Report the malaria status.
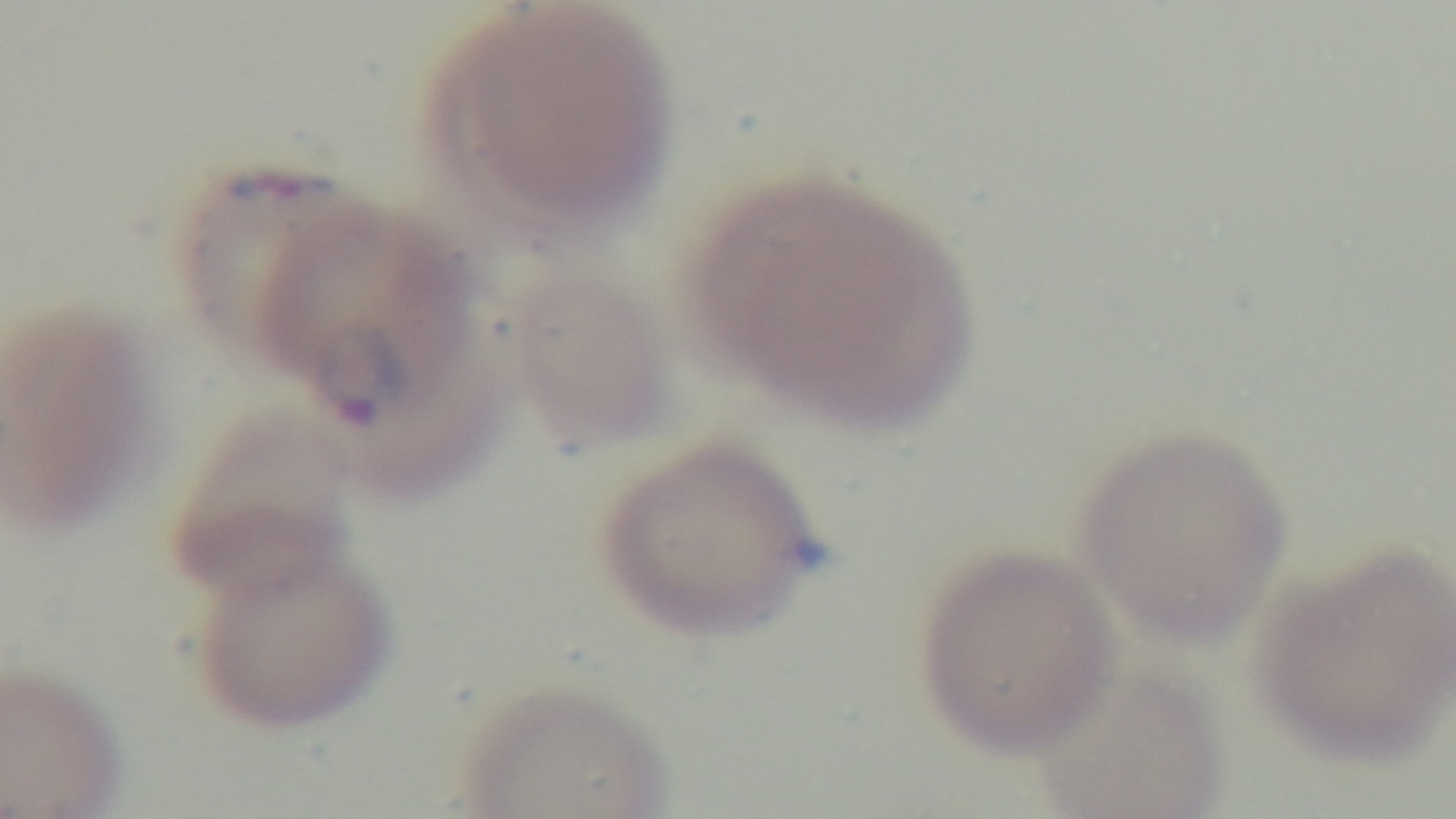

Positive.

Summary:
  - Capture: mounted 4K digital camera
  - Stain: Giemsa
  - Objective: 100x oil immersion
  - Modality: light microscopy
  - Field of view: single
  - Preparation: thin blood film